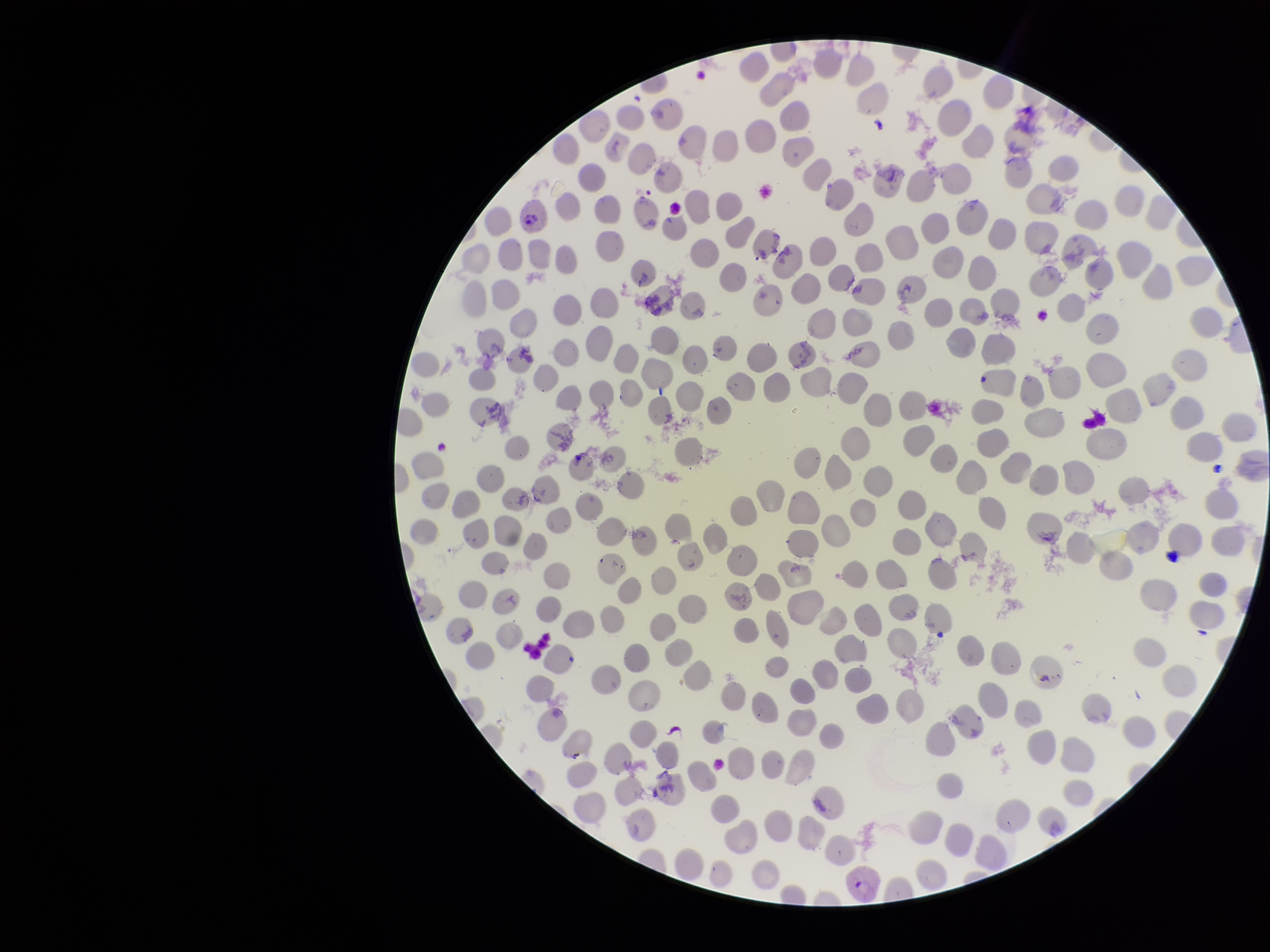

{
  "field_of_view": "single",
  "parasitized_red_blood_cell_count": 2,
  "image_size": "1270×952 pixels",
  "patient_malaria_status": "infected",
  "capture": "smartphone photograph through the microscope eyepiece",
  "preparation": "thin smear",
  "stain": "Giemsa",
  "red_blood_cell_count": 258,
  "parasitized_red_blood_cells": "identified",
  "species_reported_for_this_patient": "Plasmodium vivax"
}